Locate every Plasmodium parasite and every leukocyte.
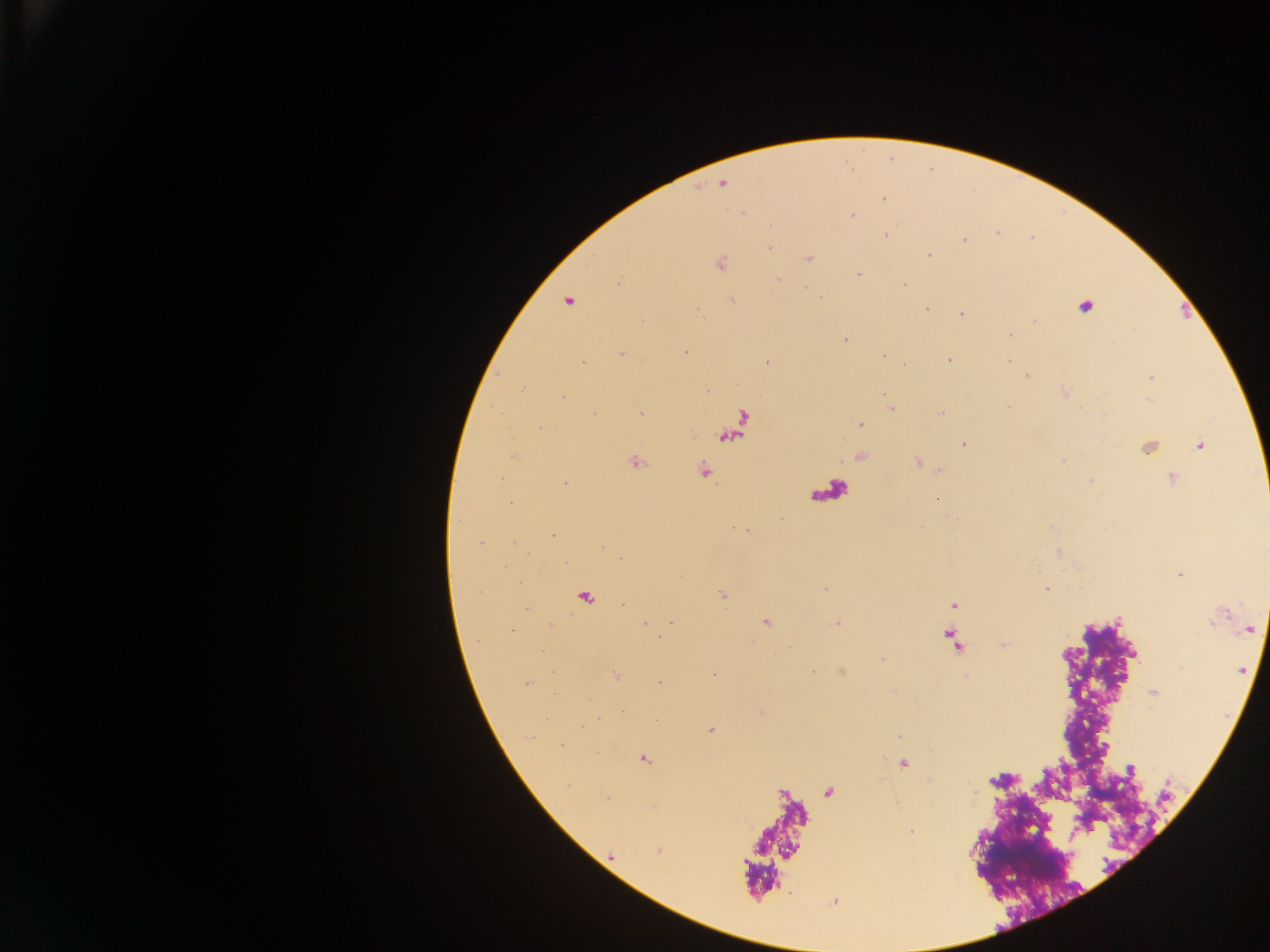

Approximate centers as (x, y) in pixels.
Plasmodium parasites: (723, 183), (884, 198), (742, 213), (852, 215), (997, 232), (886, 235), (964, 240), (770, 247), (929, 255), (809, 257), (720, 263), (859, 274), (778, 278), (905, 284), (568, 301), (732, 301), (1084, 307), (926, 309), (961, 314), (1035, 320), (1010, 334), (845, 339), (685, 352), (622, 355), (883, 356), (948, 360), (767, 362), (583, 363), (1026, 376), (1151, 378), (523, 389), (563, 397), (890, 408), (594, 413), (642, 413), (941, 413), (743, 421), (860, 424), (539, 426), (725, 439), (963, 445), (1200, 445), (513, 456), (636, 461), (1064, 461), (918, 462), (704, 470), (1172, 477), (501, 478), (1091, 481), (565, 483), (937, 498), (510, 501), (552, 536), (480, 543), (513, 543), (621, 557), (1047, 588), (826, 589), (723, 594), (586, 596), (954, 605), (526, 609), (765, 622), (672, 623), (837, 623), (645, 625), (550, 626), (1249, 629), (1004, 644), (542, 652), (883, 659), (812, 672), (714, 674), (616, 676), (661, 682), (526, 683), (1154, 692), (590, 699), (710, 730), (562, 745), (645, 759), (904, 764), (1131, 769), (828, 792), (974, 792), (606, 798), (910, 832), (659, 850), (612, 856).
No leukocytes observed.

One field of view. Image is 1270×952 pixels. Thick blood film. Collected in Ghana. Mobile-phone photograph taken through the microscope.